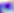 Photomicrograph. 400x magnification. Toxoplasma gondii is shown.